Locate every uninfected red blood cell.
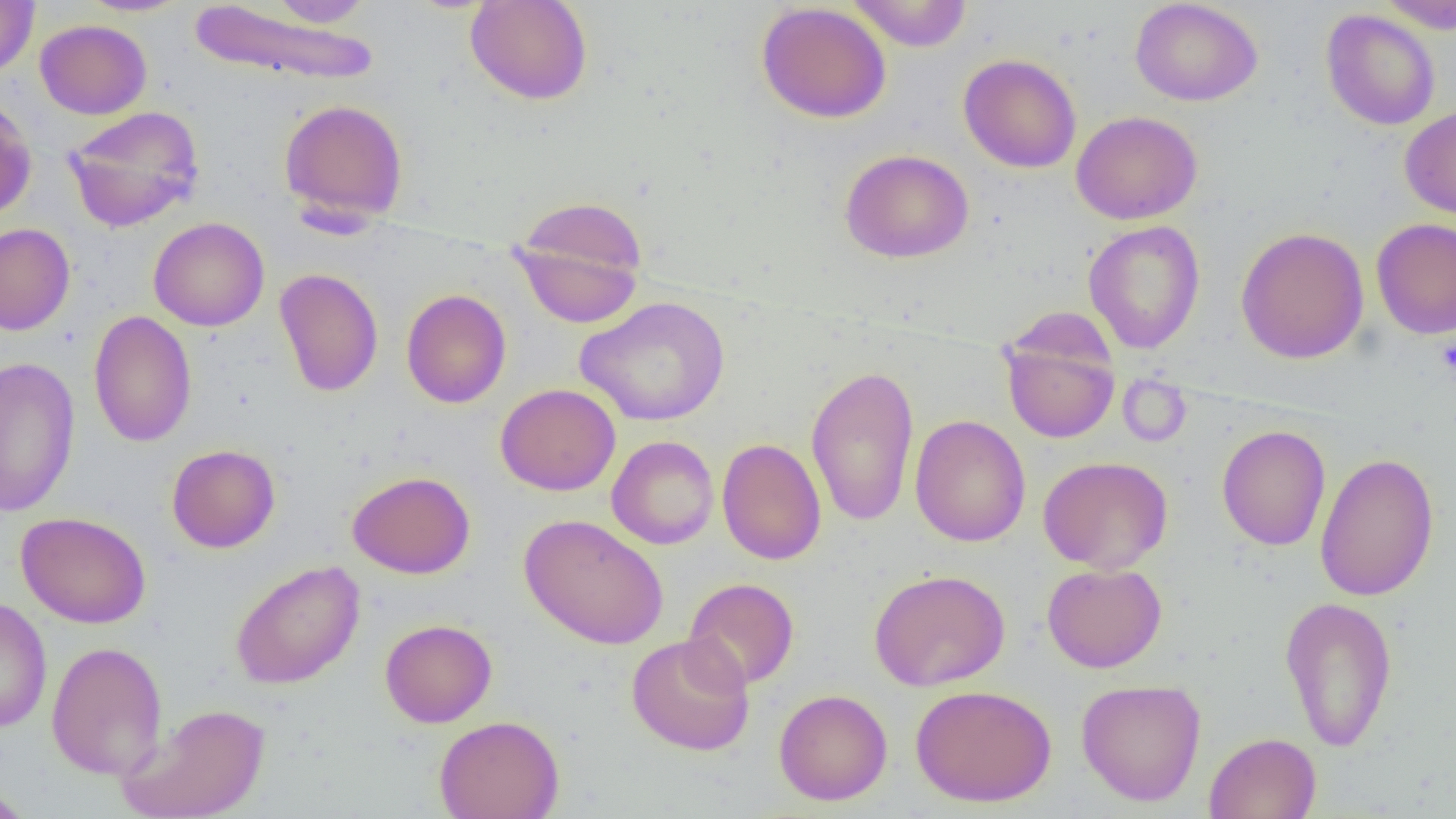

Approximate bounding boxes as [x1, y1, x2, y2] in pixels.
Uninfected red blood cells: [76, 0, 193, 17], [262, 0, 377, 28], [465, 0, 593, 105], [846, 0, 973, 52], [1130, 0, 1263, 106], [1376, 0, 1456, 33], [0, 1, 39, 79], [186, 2, 379, 86], [755, 2, 892, 123], [1320, 9, 1440, 130], [34, 18, 152, 119], [958, 53, 1082, 173], [0, 96, 37, 221], [278, 98, 410, 226], [1399, 104, 1456, 221], [63, 105, 205, 233], [1071, 110, 1202, 225], [840, 149, 974, 263], [510, 197, 648, 327], [148, 217, 270, 332], [1371, 218, 1455, 339], [1083, 220, 1205, 354], [0, 223, 75, 336], [1235, 226, 1369, 364], [274, 268, 383, 397], [401, 288, 511, 408], [575, 296, 730, 426], [88, 310, 197, 448], [1000, 325, 1120, 444], [0, 356, 80, 517], [806, 364, 920, 527], [495, 383, 621, 496], [910, 414, 1030, 547], [1216, 425, 1331, 551], [606, 435, 720, 550], [717, 437, 827, 565], [166, 444, 280, 553], [1314, 452, 1440, 601], [1038, 455, 1173, 574], [347, 471, 476, 579], [16, 511, 152, 629], [519, 513, 669, 649], [230, 560, 366, 689], [1042, 562, 1167, 673], [868, 569, 1011, 691], [683, 577, 799, 691], [0, 595, 52, 734], [1279, 596, 1398, 751], [380, 619, 498, 728], [626, 633, 755, 756], [47, 641, 167, 780], [1076, 679, 1206, 805], [910, 684, 1056, 807], [773, 689, 892, 806], [118, 702, 270, 819], [434, 715, 564, 819], [1204, 732, 1321, 819], [0, 784, 37, 818].

Platelet locations: [1436, 335, 1456, 379]. Slide-level diagnosis: no evidence of blood parasites. Thin blood film. Optical microscopy. 1000x magnification. Image is 1456×819 pixels. Single field of view.